Locate every malaria parasite.
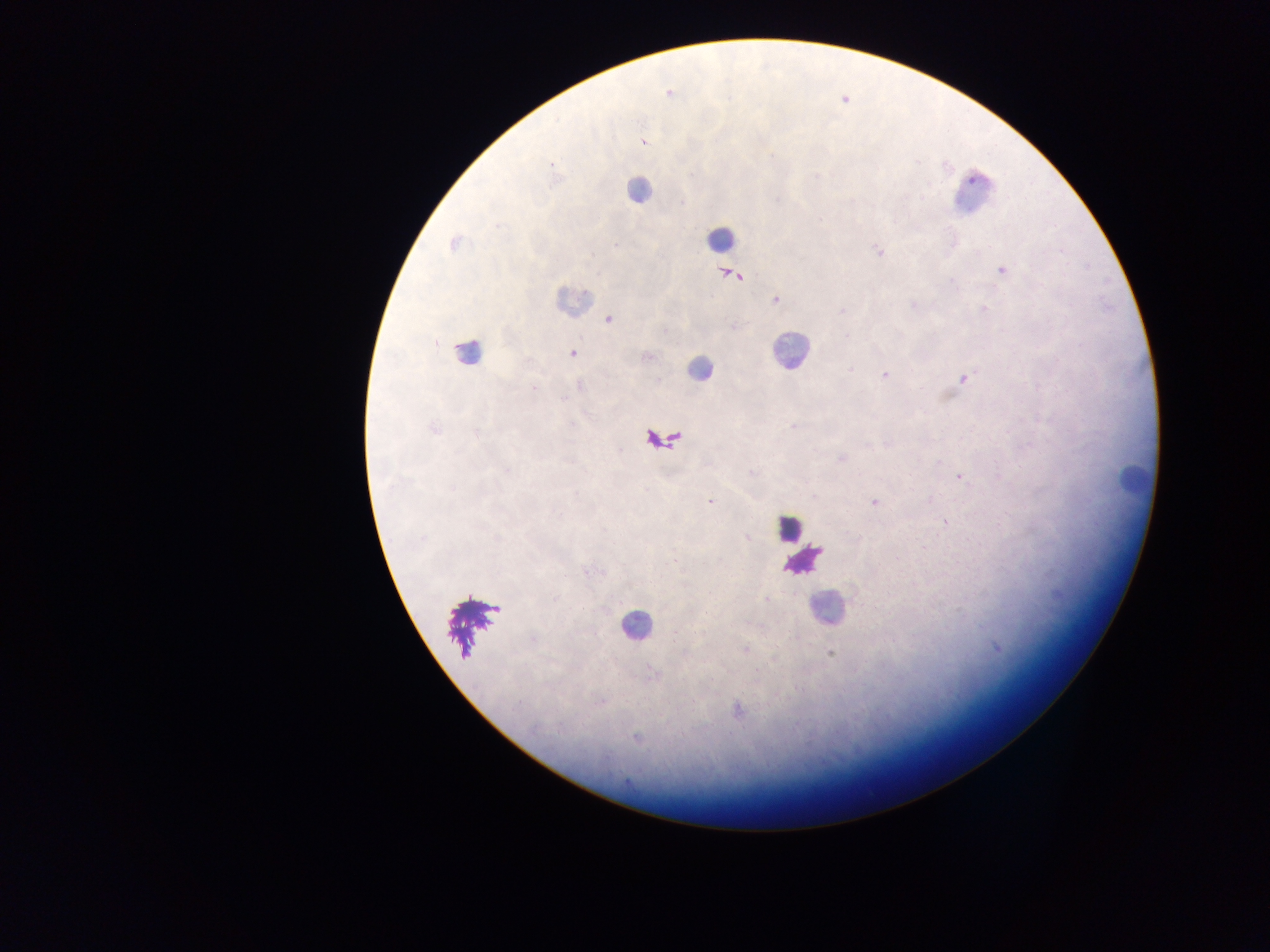

Approximate centers as [x, y] in pixels.
Malaria parasites: [668, 93], [642, 140], [551, 163], [454, 243], [879, 252], [1002, 271], [730, 275], [776, 299], [984, 309], [842, 311], [609, 319], [573, 353], [885, 375], [963, 377], [433, 429], [841, 458], [959, 477], [710, 502], [874, 502], [945, 521], [747, 537], [765, 598], [997, 648], [830, 653], [600, 701], [737, 710], [637, 738].

{
  "country": "Ghana",
  "image_size": "1270×952 pixels",
  "field_of_view": "single",
  "capture": "mobile-phone photograph through a microscope",
  "leukocyte_locations": "approximate centers as [x, y] in pixels: [636, 190], [972, 192], [719, 238], [571, 300], [467, 351], [790, 351], [699, 369], [662, 441], [1136, 480], [789, 528], [803, 560], [827, 608], [635, 627]",
  "preparation": "thick blood film"
}